Comment on the morphology of the red blood cells.
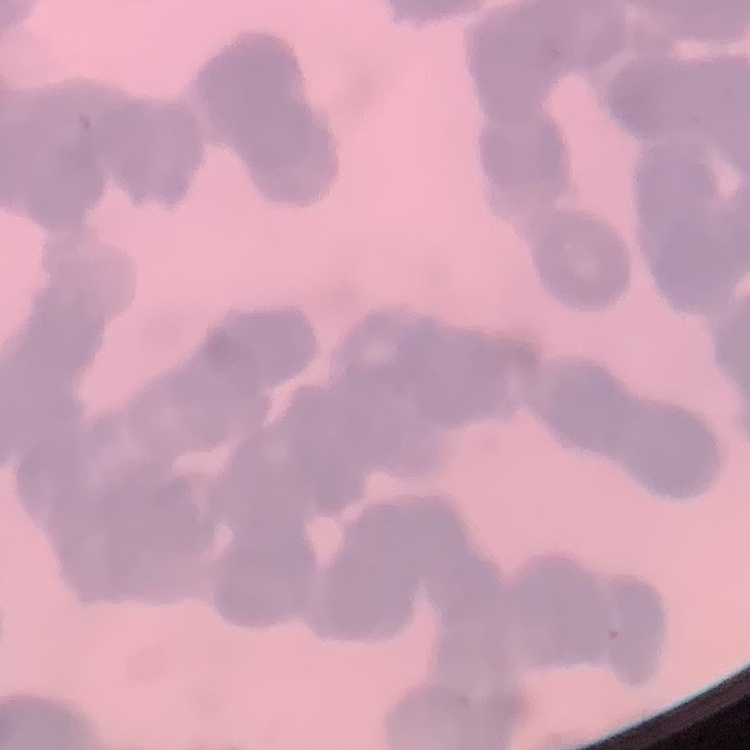
Rouleaux formation.

Summary:
  - Stain: Field's or Giemsa
  - Image type: square crop of a larger photomicrograph
  - Preparation: thin blood smear